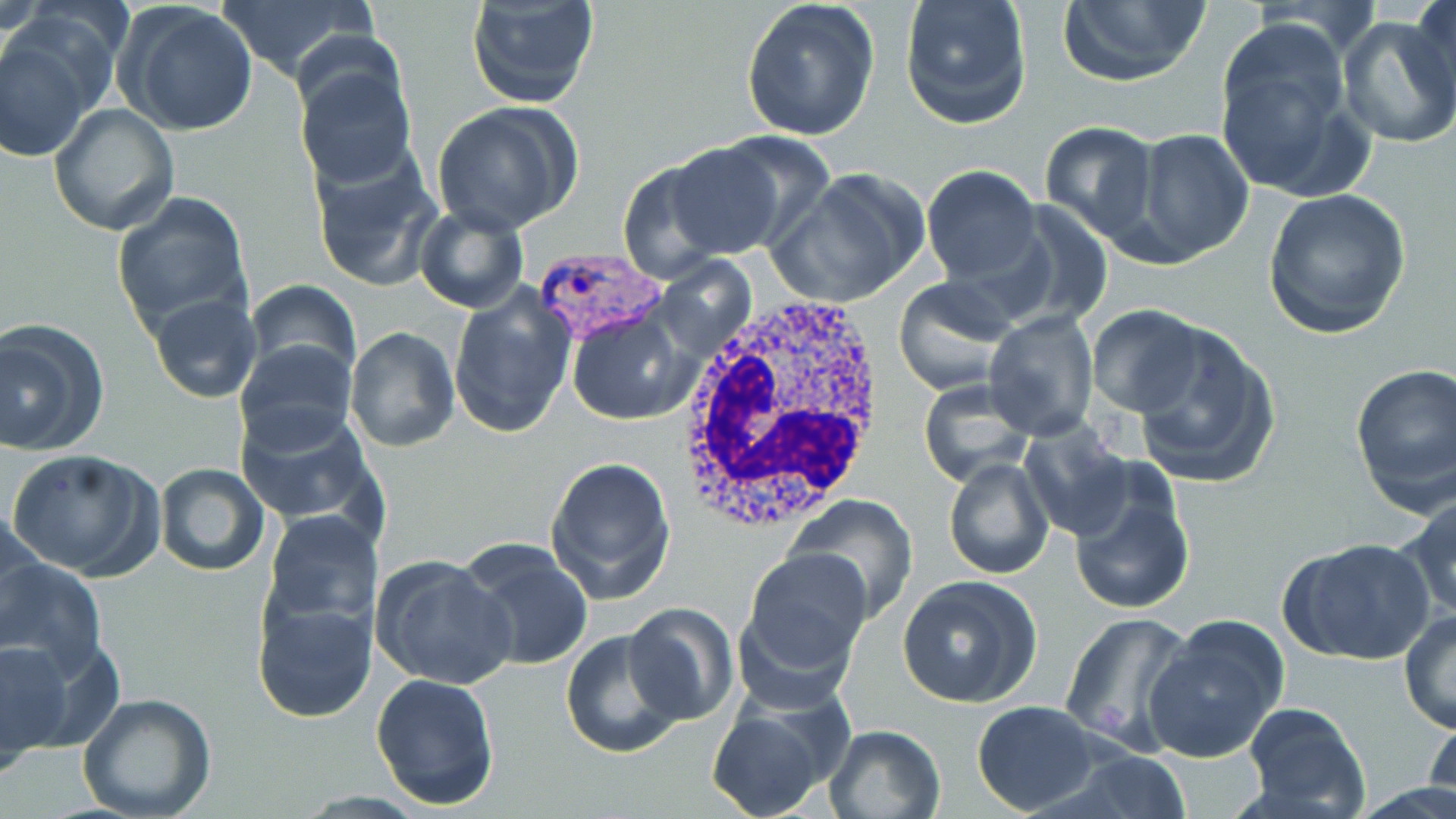 Approximate bounding boxes as [x1, y1, x2, y2] in pixels. White blood cell locations: [672, 289, 886, 533]. Plasmodium vivax-infected red blood cell locations: [540, 252, 668, 344]. Uninfected red blood cell locations: [208, 0, 378, 84], [465, 0, 600, 108], [739, 0, 881, 142], [899, 0, 1033, 130], [1054, 0, 1212, 87], [1409, 1, 1456, 111], [120, 4, 260, 138], [1336, 12, 1456, 152], [1213, 20, 1370, 198], [0, 28, 97, 162], [294, 63, 417, 189], [432, 102, 584, 235], [48, 103, 180, 235], [1038, 121, 1162, 243], [1129, 128, 1254, 263], [702, 131, 839, 252], [663, 141, 787, 258], [309, 149, 443, 294], [616, 158, 735, 284], [920, 165, 1042, 285], [771, 168, 924, 308], [1261, 189, 1412, 339], [112, 192, 253, 337], [991, 202, 1112, 331], [413, 203, 530, 315], [892, 276, 1021, 397], [246, 280, 360, 381], [447, 286, 579, 440], [146, 294, 262, 405], [1088, 304, 1208, 416], [566, 311, 695, 424], [983, 312, 1099, 438], [1125, 320, 1282, 490], [0, 321, 109, 455], [345, 327, 460, 452], [234, 337, 359, 451], [1349, 362, 1456, 512], [917, 383, 1033, 488], [235, 405, 381, 532], [1018, 419, 1132, 541], [7, 447, 161, 580], [544, 455, 677, 604], [944, 457, 1054, 579], [153, 463, 270, 577], [1067, 465, 1197, 616], [1397, 492, 1456, 623], [784, 493, 919, 622], [2, 503, 50, 646], [261, 509, 382, 633], [1284, 536, 1436, 667], [457, 539, 595, 673], [741, 547, 873, 674], [372, 553, 517, 689], [1, 556, 105, 678], [897, 575, 1042, 708], [250, 594, 378, 724], [623, 604, 739, 726], [1399, 610, 1456, 734], [1060, 611, 1196, 756], [1142, 616, 1289, 763], [560, 629, 688, 759], [0, 638, 84, 761], [370, 672, 500, 812], [76, 692, 218, 819], [706, 696, 845, 818], [972, 700, 1102, 815], [1241, 703, 1371, 818], [1423, 706, 1456, 811], [823, 723, 948, 819], [1072, 749, 1193, 818]. Slide-level diagnosis: Plasmodium vivax. May-Grünwald-Giemsa-stained preparation. Light microscopy. One field of a larger specimen. Image is 1456×819 pixels. Thin blood smear. Captured at 1000x magnification.